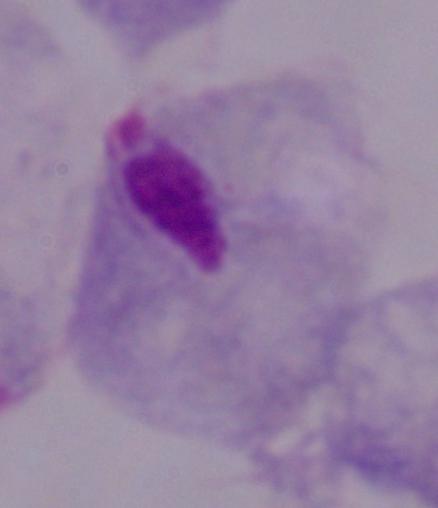
modality: micrograph
identification: trichomonad
magnification: 1000x